Identify the parasite.
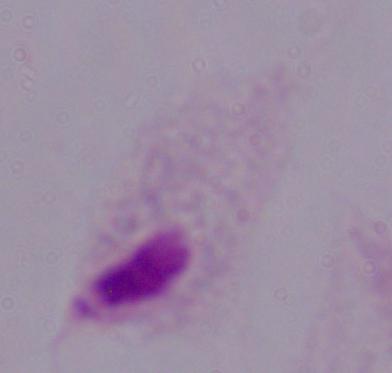
This is a trichomonad.

Summary:
  - Modality: photomicrograph
  - Magnification: 1000x